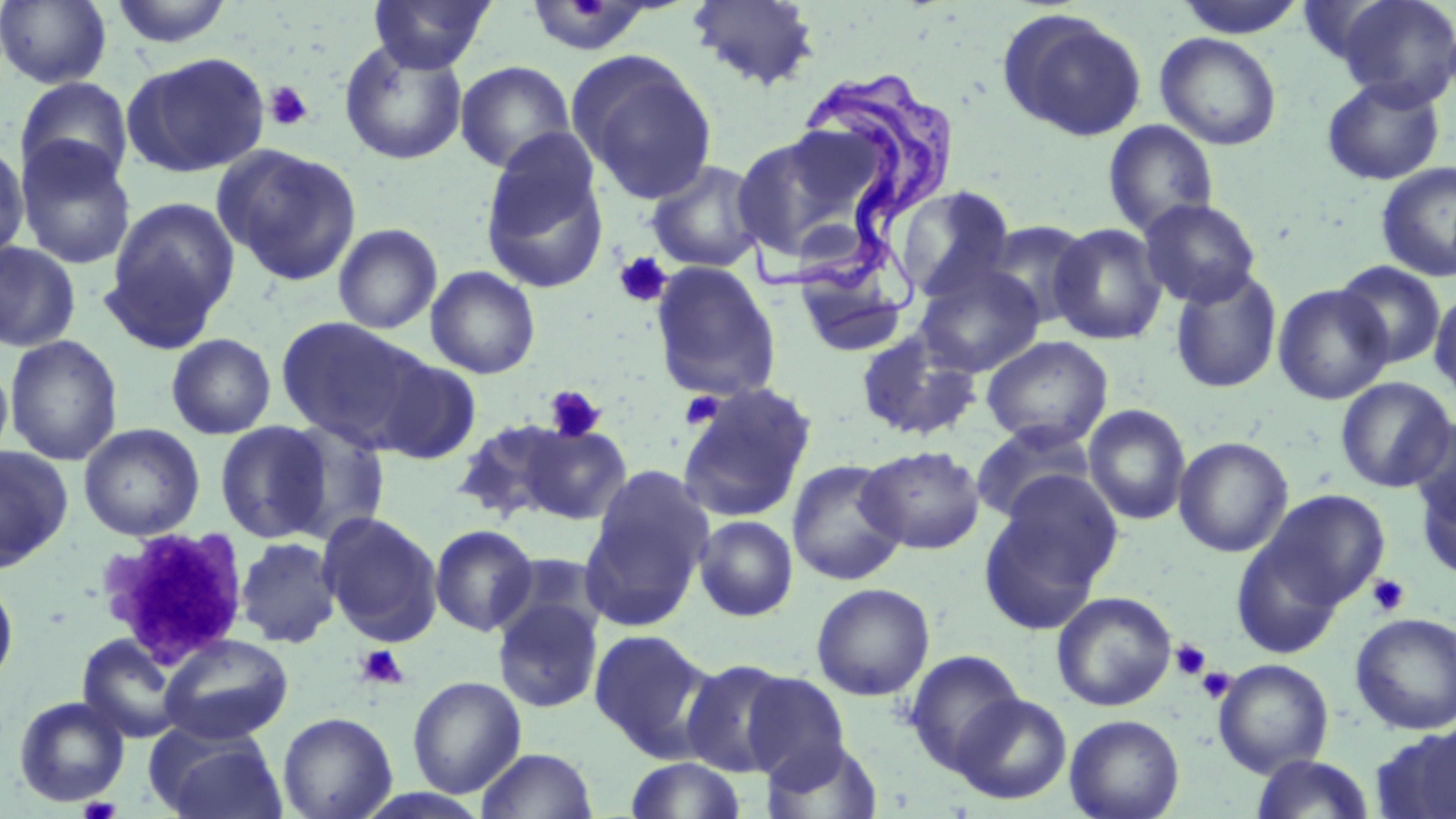
slide_level_diagnosis: Trypanosoma brucei
preparation: thin blood film
platelet_locations: 'approximate bounding boxes as (x1,y1)-(x2,y2) corner pairs in pixels: (264,80)-(313,131), (613,252)-(671,308), (544,385)-(606,443), (679,390)-(725,431), (96,533)-(243,660), (1366,574)-(1410,617), (1171,638)-(1213,681), (355,644)-(410,689), (1196,667)-(1235,704), (78,797)-(120,819)'
image_size: 1456×819 pixels
field_of_view: single
stain: May-Grünwald-Giemsa
uninfected_red_blood_cell_locations: 'approximate bounding boxes as (x1,y1)-(x2,y2) corner pairs in pixels: (0,0)-(113,89), (109,0)-(235,49), (368,0)-(495,73), (686,0)-(822,91), (1173,0)-(1308,38), (1332,0)-(1456,108), (523,2)-(658,57), (998,9)-(1148,142), (1155,32)-(1282,151), (339,41)-(467,165), (568,50)-(718,204), (124,51)-(269,178), (454,60)-(576,174), (15,76)-(133,187), (1321,77)-(1446,186), (1102,119)-(1219,237), (731,126)-(890,269), (15,137)-(137,270), (479,137)-(611,295), (0,140)-(30,265), (217,145)-(362,286), (646,159)-(767,273), (1375,161)-(1456,282), (893,185)-(1018,303), (102,196)-(240,348), (1138,198)-(1261,308), (979,220)-(1094,328), (332,223)-(442,335), (1048,223)-(1168,345), (0,241)-(81,352), (649,261)-(782,401), (1333,261)-(1447,369), (914,263)-(1045,378), (425,266)-(541,379), (1169,266)-(1283,394), (791,267)-(910,359), (1273,284)-(1393,405), (1429,289)-(1456,403), (275,315)-(431,451), (855,327)-(983,441), (166,333)-(276,440), (4,335)-(123,466), (981,335)-(1113,449), (0,356)-(14,472), (373,357)-(482,465), (1335,377)-(1455,492), (677,384)-(815,523), (1083,404)-(1192,525), (1408,416)-(1456,530), (453,418)-(573,523), (275,419)-(391,544), (214,420)-(332,543), (970,422)-(1096,524), (78,423)-(205,541), (520,423)-(632,525), (1173,436)-(1293,557), (0,445)-(74,572), (857,445)-(986,554), (787,459)-(906,585), (581,469)-(713,628), (1415,472)-(1456,582), (979,478)-(1122,634), (1259,489)-(1390,609), (318,511)-(443,646), (693,515)-(798,621), (429,524)-(538,637), (1230,533)-(1345,658), (235,537)-(342,648), (0,574)-(19,691), (811,582)-(935,701), (1051,591)-(1177,711), (492,597)-(604,714), (1350,612)-(1455,735), (588,628)-(715,759), (76,634)-(188,743), (159,634)-(293,744), (904,649)-(1024,773), (680,659)-(796,777), (1213,659)-(1334,777), (740,672)-(852,784), (407,676)-(526,798), (950,693)-(1072,805), (13,696)-(130,808), (277,711)-(397,819), (1064,714)-(1185,819), (1372,728)-(1456,818), (150,730)-(288,819), (761,737)-(884,819), (475,747)-(598,819), (1250,753)-(1375,818), (625,757)-(746,818)'
magnification: 1000x
trypanosoma_brucei_locations: 'approximate bounding boxes as (x1,y1)-(x2,y2) corner pairs in pixels: (738,63)-(957,339)'
modality: optical microscopy